Comment on the morphology of the erythrocytes.
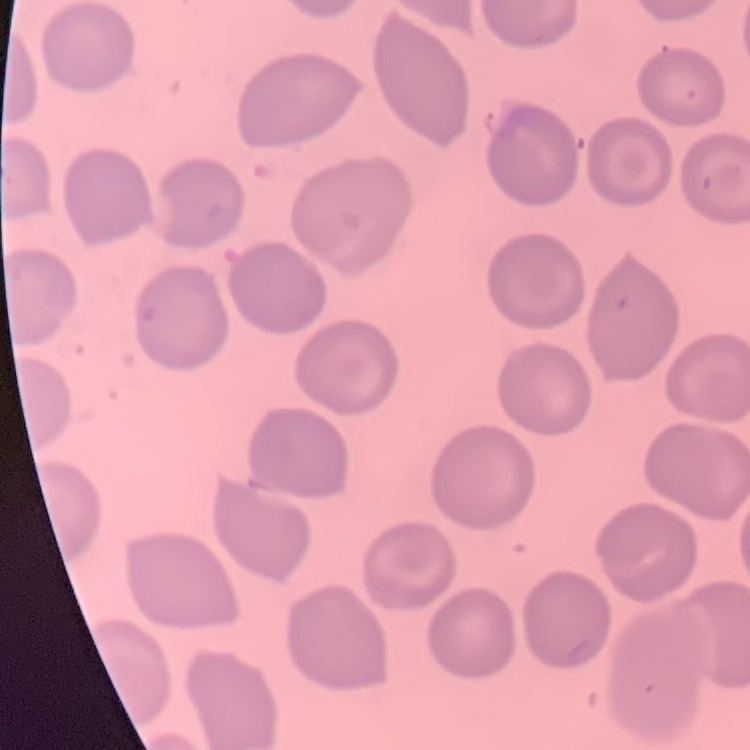
No rouleaux formation.

One tile cut from a larger photomicrograph. Field's or Giemsa stain. Thin blood film.